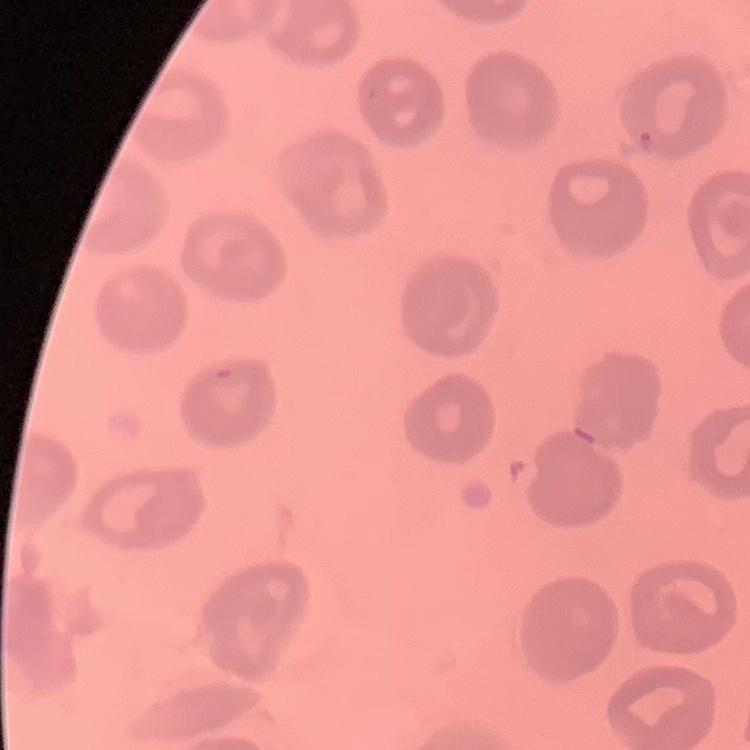

The red blood cells show no rouleaux formation. Stained with either Field's or Giemsa. One tile cut from a larger photomicrograph. Thin blood film.